Report the malaria status of this cell.
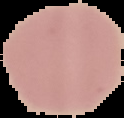

Uninfected.

image size = 124×118 pixels
preparation = thin blood film
image type = segmented cell region with the area outside set to black